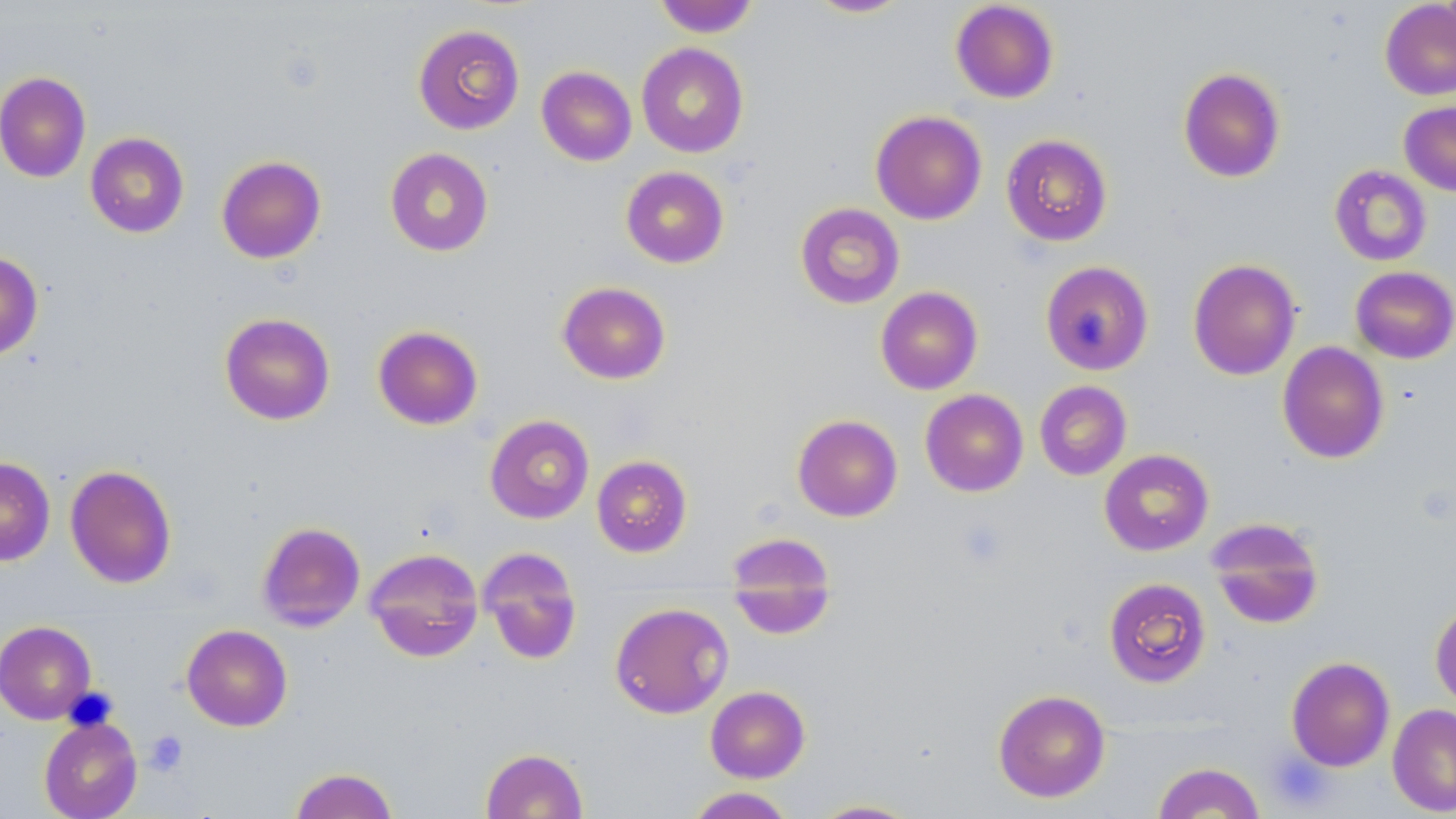

slide-level diagnosis = no evidence of blood parasites
preparation = thin blood smear
modality = optical microscopy
field of view = one of a larger specimen
platelet locations = approximate bounding boxes as (x1, y1, x2, y2) in pixels: (955, 519, 1010, 570), (144, 730, 188, 776)
magnification = 1000x
stain = May-Grünwald-Giemsa
uninfected red blood cell locations = approximate bounding boxes as (x1, y1, x2, y2) in pixels: (653, 0, 760, 37), (805, 0, 913, 18), (950, 1, 1059, 103), (1379, 1, 1456, 100), (413, 24, 525, 135), (636, 43, 749, 157), (536, 66, 636, 166), (1177, 67, 1286, 183), (0, 72, 91, 183), (1399, 101, 1456, 196), (870, 110, 987, 225), (85, 132, 189, 237), (1001, 133, 1113, 246), (384, 147, 494, 257), (216, 155, 326, 264), (1329, 164, 1432, 266), (620, 166, 729, 268), (795, 202, 905, 309), (0, 251, 43, 360), (1188, 258, 1301, 380), (1040, 260, 1154, 376), (1350, 266, 1456, 364), (556, 281, 671, 384), (875, 286, 983, 395), (219, 312, 336, 425), (372, 325, 484, 430), (1277, 341, 1390, 463), (1034, 380, 1132, 481), (920, 389, 1029, 497), (485, 414, 594, 524), (792, 414, 903, 522), (1099, 449, 1214, 556), (591, 455, 692, 557), (0, 456, 55, 566), (64, 464, 177, 589), (1206, 517, 1325, 630), (256, 521, 366, 632), (725, 532, 838, 640), (477, 546, 583, 665), (364, 547, 484, 662), (1103, 577, 1212, 688), (1430, 601, 1456, 710), (609, 602, 733, 719), (0, 620, 97, 724), (181, 624, 292, 731), (1286, 656, 1395, 772), (705, 686, 811, 782), (993, 688, 1111, 802), (1387, 703, 1456, 816), (38, 715, 143, 819), (481, 747, 588, 819), (1152, 761, 1265, 818), (289, 767, 399, 819), (685, 787, 797, 818), (808, 799, 921, 818)
image size = 1456×819 pixels